Identify the cell.
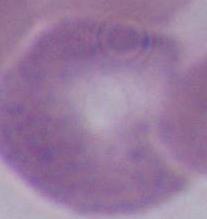

This is an erythrocyte.

Photomicrograph. 1000x magnification.